Locate leukocytes (white blood cells).
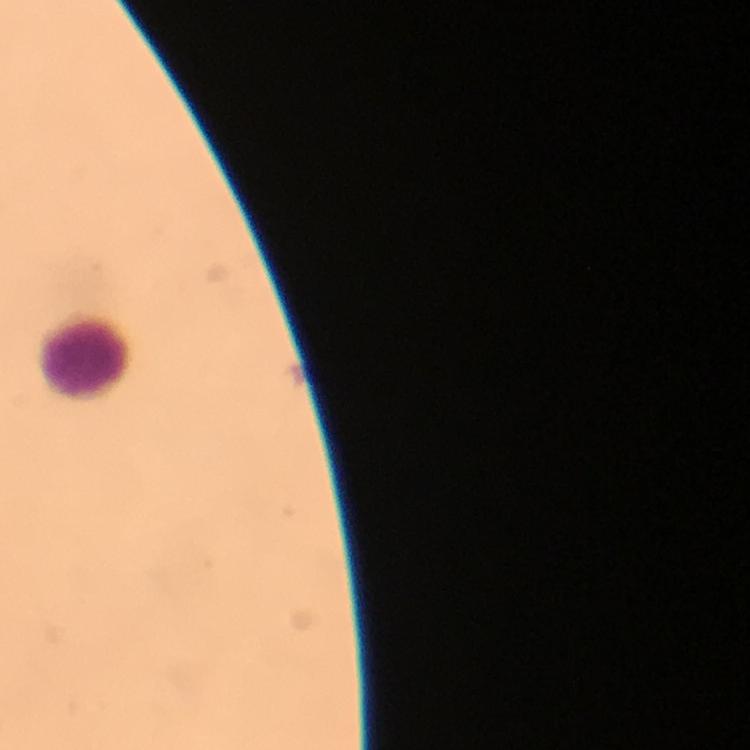
Approximate object centers, in pixels from the top-left corner.
Leukocytes: (x=88, y=360).

Immersion oil was used. Thick smear. At 100x magnification. Image is 750×750 pixels. Photographed through the microscope with a smartphone camera. Giemsa-stained preparation. Malaria parasites: none detected. From a diagnostic examination for malaria. A crop from one field of view.